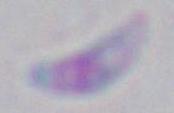

Summary:
  - Magnification: 1000x
  - Modality: micrograph
  - Identification: Toxoplasma gondii